Report the malaria status of this cell.
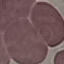

It is uninfected.

{
  "stain": "Giemsa",
  "image_type": "cell patch, automatically extracted from a larger field of view and resized to 64 × 64 pixels",
  "capture": "smartphone through the microscope eyepiece",
  "preparation": "thin blood smear"
}